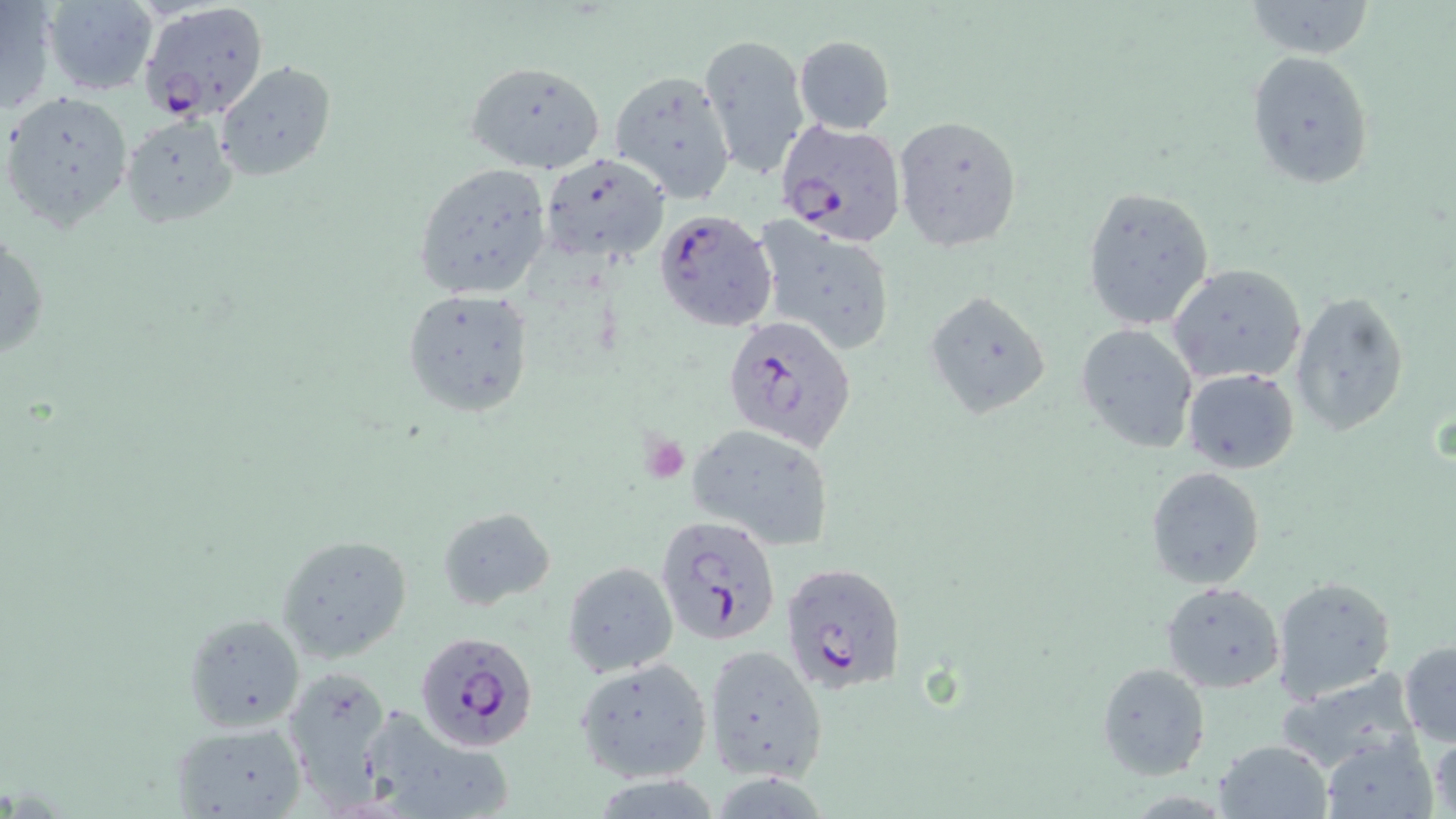
Summary:
  - Coordinate format: approximate bounding boxes as [x1, y1, x2, y2] in pixels
  - Plasmodium falciparum-infected red blood cell locations: [138, 2, 270, 121], [775, 119, 907, 245], [654, 209, 778, 333], [723, 314, 857, 452], [656, 515, 781, 643], [778, 561, 907, 696], [416, 631, 542, 754]
  - Uninfected red blood cell locations: [39, 0, 158, 96], [1, 1, 56, 114], [1243, 1, 1378, 59], [699, 33, 812, 183], [794, 36, 895, 133], [1245, 51, 1373, 190], [215, 61, 336, 183], [465, 61, 607, 174], [608, 68, 738, 204], [2, 89, 133, 230], [892, 113, 1024, 251], [120, 115, 239, 228], [539, 152, 670, 267], [412, 162, 554, 300], [1082, 187, 1216, 331], [756, 223, 895, 356], [0, 231, 48, 362], [1167, 264, 1308, 387], [400, 289, 533, 416], [925, 289, 1051, 417], [1291, 290, 1411, 439], [1076, 324, 1197, 453], [1182, 368, 1300, 475], [684, 422, 837, 552], [1145, 466, 1266, 590], [437, 506, 556, 611], [275, 533, 414, 664], [562, 560, 678, 680], [1272, 577, 1396, 702], [1161, 580, 1285, 693], [182, 614, 304, 731], [1399, 640, 1456, 745], [702, 643, 829, 781], [573, 658, 712, 784], [1097, 662, 1211, 781], [281, 667, 395, 805], [1276, 667, 1423, 770], [371, 712, 512, 810], [167, 721, 309, 819], [1427, 726, 1455, 818], [1318, 734, 1437, 818], [1213, 739, 1334, 819]
  - Slide-level diagnosis: Plasmodium falciparum
  - Stain: May-Grünwald-Giemsa
  - Field of view: single
  - Preparation: thin blood film
  - Modality: light microscopy
  - Image size: 1456×819 pixels
  - Magnification: 1000x